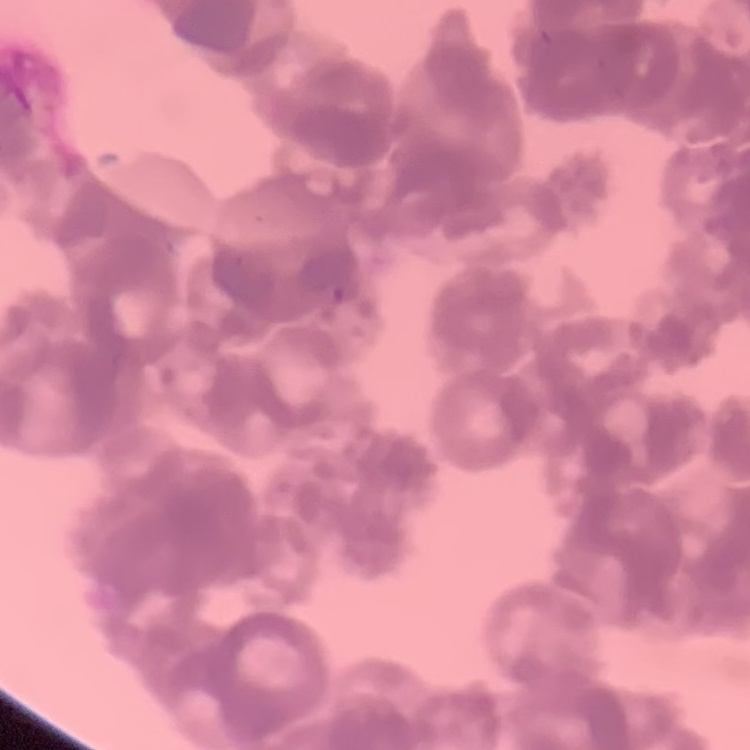

Summary:
  - Erythrocyte morphology: rouleaux formation
  - Image type: square crop of a larger photomicrograph
  - Stain: Field's or Giemsa
  - Preparation: thin blood smear